Name the parasite shown.
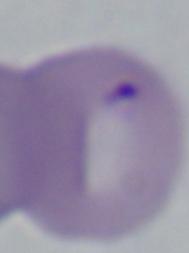
This is Babesia.

magnification: 1000x
modality: micrograph